Assess this cell for malaria.
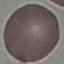
It is uninfected.

Summary:
  - Stain: Giemsa
  - Preparation: thin blood smear
  - Capture: smartphone camera at the microscope eyepiece
  - Image type: automatically extracted cell patch, resized to 64 × 64 pixels